Report the malaria status of this cell.
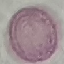
Uninfected.

Photographed with a smartphone camera at the microscope eyepiece. Giemsa-stained preparation. Thin smear of blood. Cell patch, automatically extracted from a larger field of view and resized to 64 × 64 pixels.